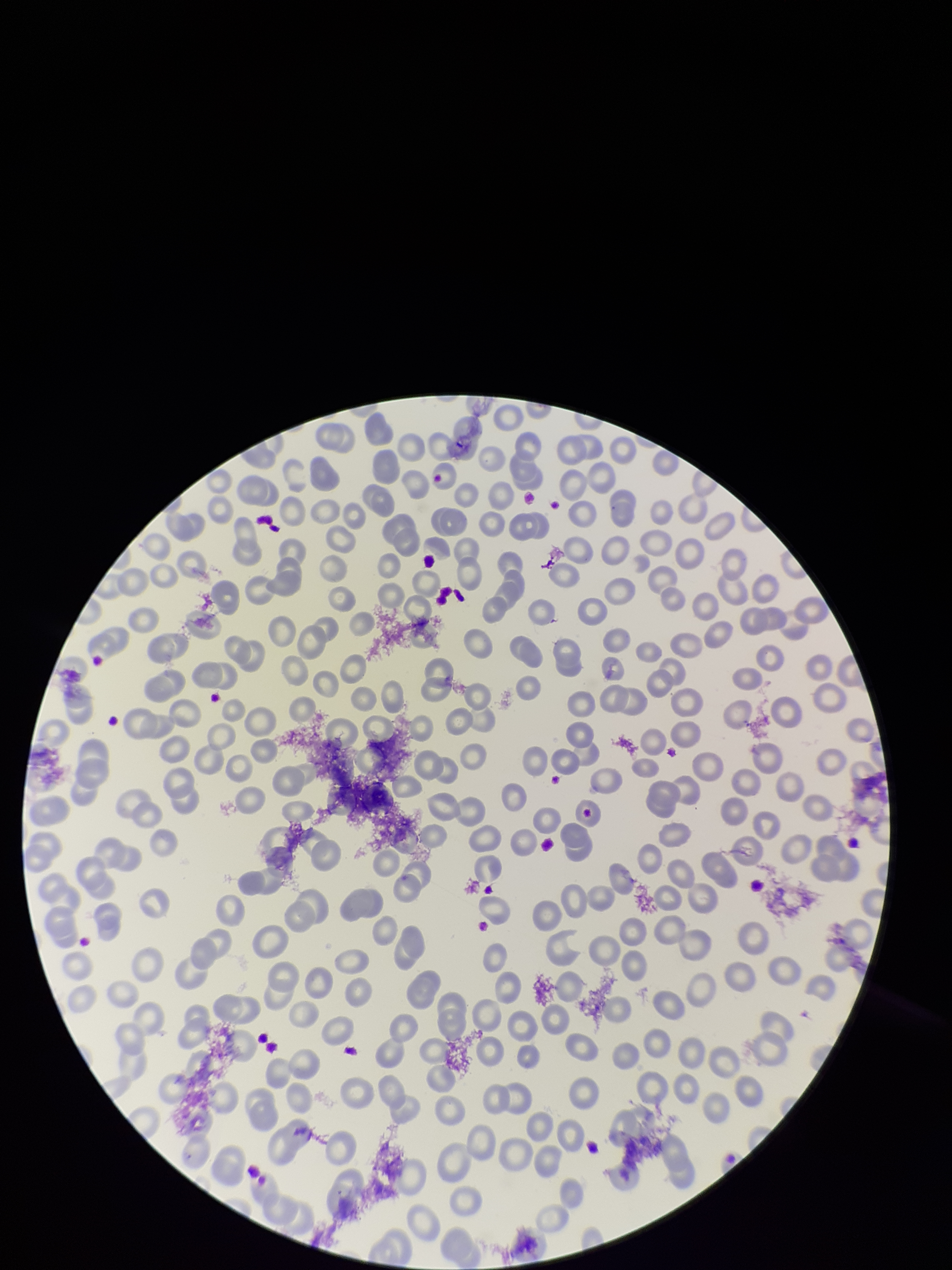
Giemsa stain. One field from this slide. Smartphone photograph taken through the eyepiece of a microscope. Species reported for this patient: Plasmodium falciparum. Parasitized red blood cells: none seen. Preparation: thin blood smear. Parasitized red blood cell count: 0. Patient malaria status: infected. Red blood cell count: 244. Image is 952×1270 pixels.